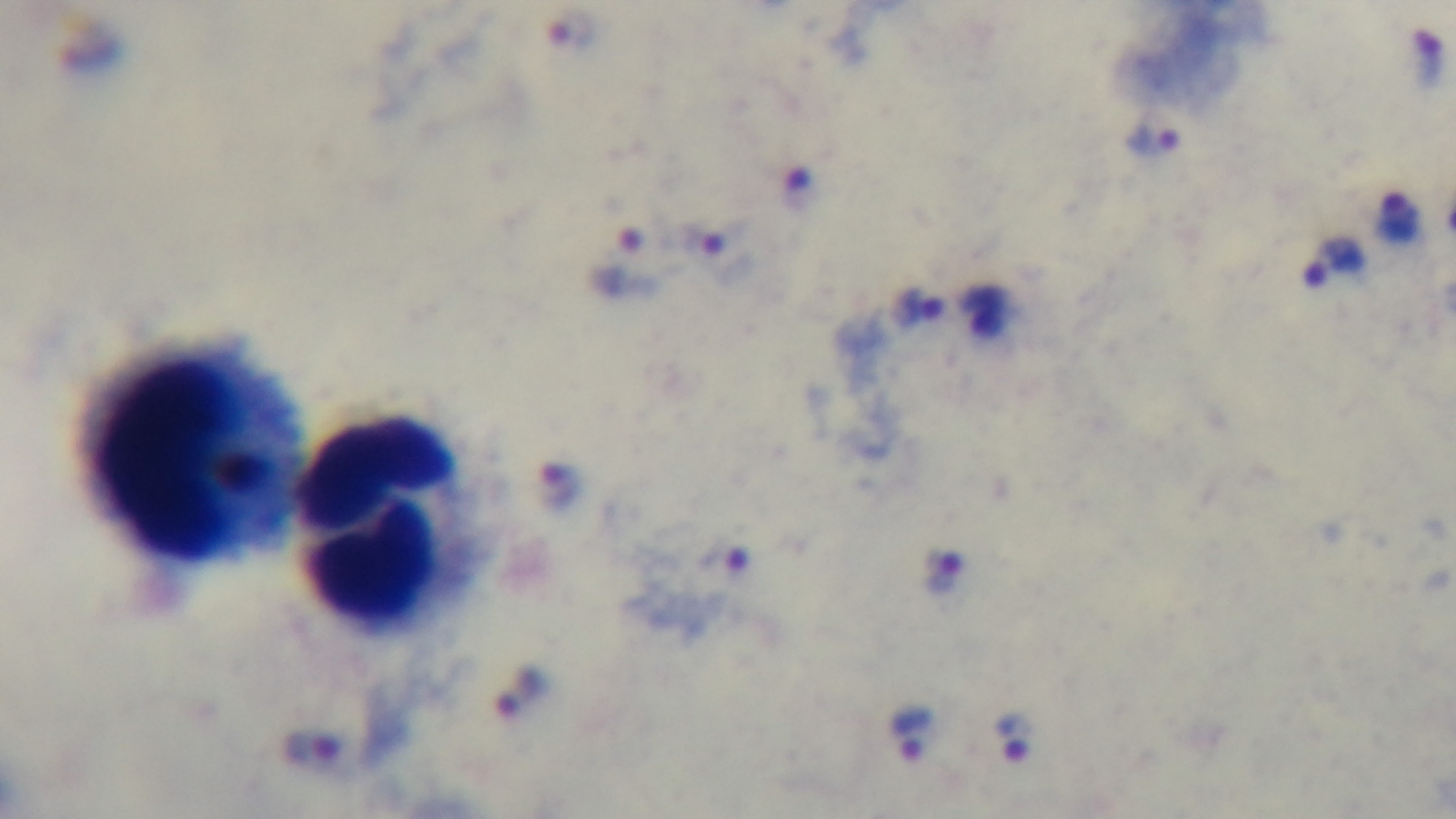
Mounted 4K digital camera. Giemsa stain. Malaria status: positive. One field from the slide. Preparation: thick blood film. Oil-immersion objective, 100x. Photomicrograph.